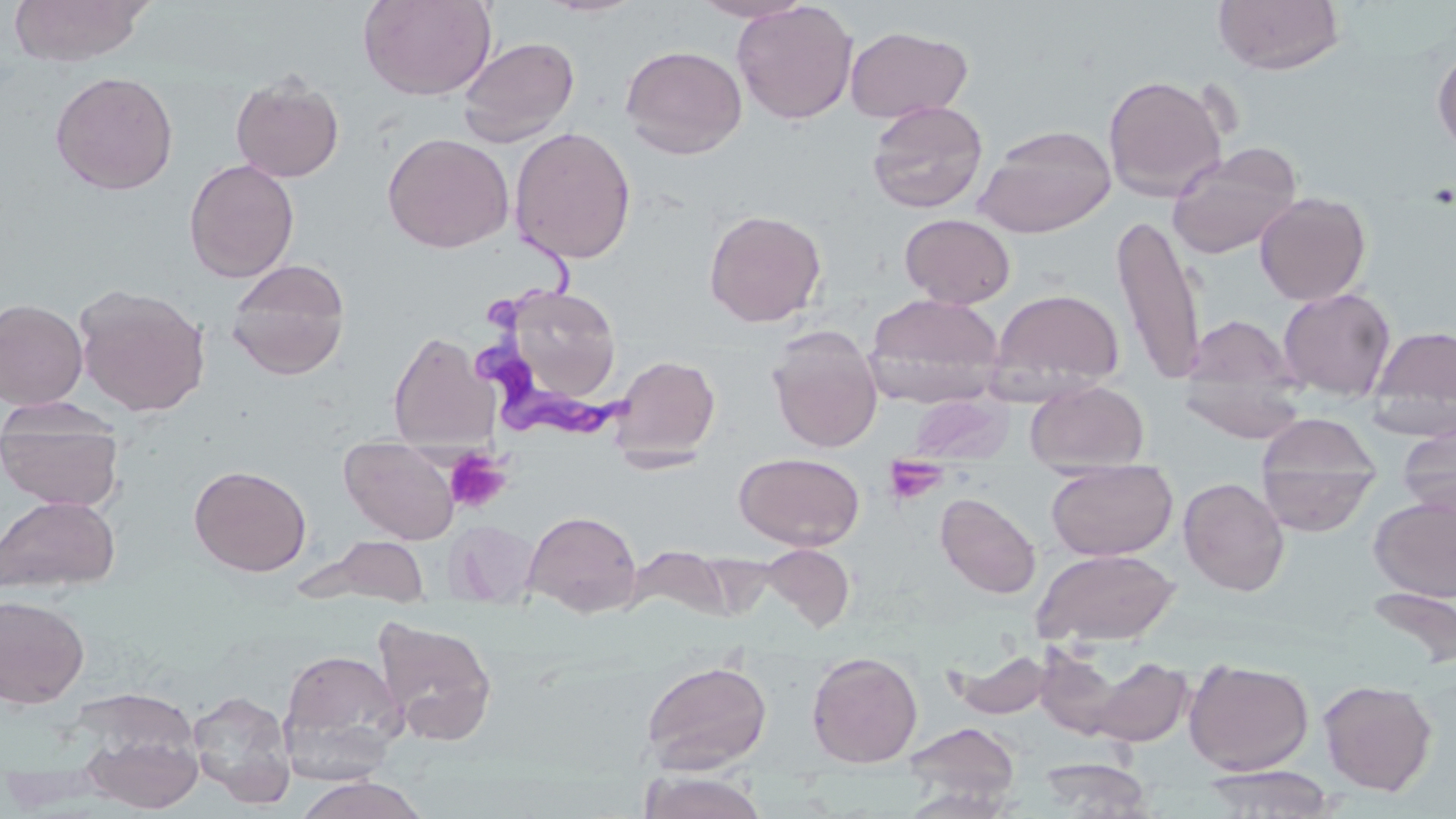

Summary:
  - Coordinate format: approximate bounding boxes as named x1/y1/x2/y2 corners in pixels
  - Trypanosoma brucei locations: (x1=477, y1=239, x2=631, y2=439)
  - Platelet locations: (x1=445, y1=449, x2=511, y2=513), (x1=882, y1=454, x2=948, y2=507)
  - Uninfected red blood cell locations: (x1=6, y1=0, x2=152, y2=66), (x1=358, y1=0, x2=497, y2=101), (x1=537, y1=0, x2=646, y2=18), (x1=691, y1=0, x2=814, y2=22), (x1=1213, y1=0, x2=1345, y2=75), (x1=732, y1=1, x2=858, y2=125), (x1=845, y1=25, x2=973, y2=124), (x1=457, y1=35, x2=580, y2=146), (x1=620, y1=44, x2=747, y2=159), (x1=1432, y1=47, x2=1456, y2=156), (x1=49, y1=70, x2=179, y2=195), (x1=230, y1=74, x2=345, y2=183), (x1=1103, y1=74, x2=1228, y2=200), (x1=866, y1=101, x2=988, y2=214), (x1=974, y1=124, x2=1117, y2=237), (x1=509, y1=126, x2=637, y2=265), (x1=382, y1=132, x2=514, y2=253), (x1=1167, y1=143, x2=1303, y2=259), (x1=183, y1=158, x2=300, y2=283), (x1=1255, y1=191, x2=1371, y2=305), (x1=703, y1=208, x2=827, y2=327), (x1=900, y1=213, x2=1016, y2=309), (x1=1113, y1=213, x2=1206, y2=386), (x1=226, y1=260, x2=351, y2=380), (x1=74, y1=283, x2=211, y2=417), (x1=490, y1=283, x2=626, y2=412), (x1=989, y1=288, x2=1125, y2=397), (x1=1277, y1=288, x2=1396, y2=401), (x1=864, y1=294, x2=1005, y2=407), (x1=0, y1=298, x2=88, y2=410), (x1=1181, y1=314, x2=1298, y2=399), (x1=1368, y1=324, x2=1456, y2=434), (x1=767, y1=326, x2=883, y2=453), (x1=387, y1=331, x2=497, y2=449), (x1=609, y1=354, x2=721, y2=463), (x1=1179, y1=371, x2=1308, y2=443), (x1=1026, y1=380, x2=1149, y2=472), (x1=909, y1=394, x2=1009, y2=464), (x1=1, y1=401, x2=123, y2=512), (x1=1255, y1=415, x2=1382, y2=533), (x1=1397, y1=421, x2=1456, y2=520), (x1=340, y1=440, x2=459, y2=545), (x1=734, y1=451, x2=865, y2=550), (x1=1045, y1=459, x2=1177, y2=561), (x1=189, y1=464, x2=311, y2=576), (x1=1178, y1=477, x2=1290, y2=596), (x1=936, y1=492, x2=1041, y2=599), (x1=0, y1=495, x2=120, y2=595), (x1=1369, y1=495, x2=1456, y2=601), (x1=523, y1=509, x2=643, y2=618), (x1=445, y1=520, x2=540, y2=608), (x1=331, y1=535, x2=430, y2=605), (x1=761, y1=543, x2=855, y2=632), (x1=633, y1=545, x2=733, y2=621), (x1=1033, y1=548, x2=1180, y2=647), (x1=1366, y1=585, x2=1456, y2=671), (x1=0, y1=594, x2=90, y2=708), (x1=372, y1=616, x2=498, y2=746), (x1=1033, y1=642, x2=1154, y2=743), (x1=277, y1=647, x2=407, y2=779), (x1=947, y1=648, x2=1054, y2=720), (x1=806, y1=650, x2=923, y2=768), (x1=1077, y1=654, x2=1197, y2=747), (x1=641, y1=658, x2=772, y2=774), (x1=1184, y1=658, x2=1314, y2=775), (x1=1318, y1=678, x2=1437, y2=796), (x1=187, y1=689, x2=296, y2=807), (x1=78, y1=718, x2=205, y2=813), (x1=902, y1=721, x2=1020, y2=808), (x1=1037, y1=755, x2=1155, y2=817), (x1=1196, y1=765, x2=1340, y2=817), (x1=640, y1=770, x2=768, y2=819), (x1=293, y1=776, x2=430, y2=819)
  - Slide-level diagnosis: Trypanosoma brucei
  - Stain: May-Grünwald-Giemsa
  - Modality: optical microscopy
  - Field of view: one of a larger specimen
  - Image size: 1456×819 pixels
  - Preparation: thin blood smear
  - Magnification: 1000x